Name the parasite shown.
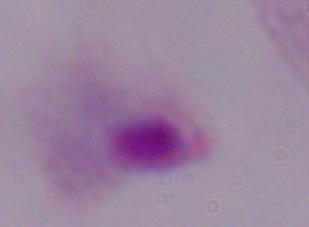

A trichomonad.

Micrograph. 1000x magnification.